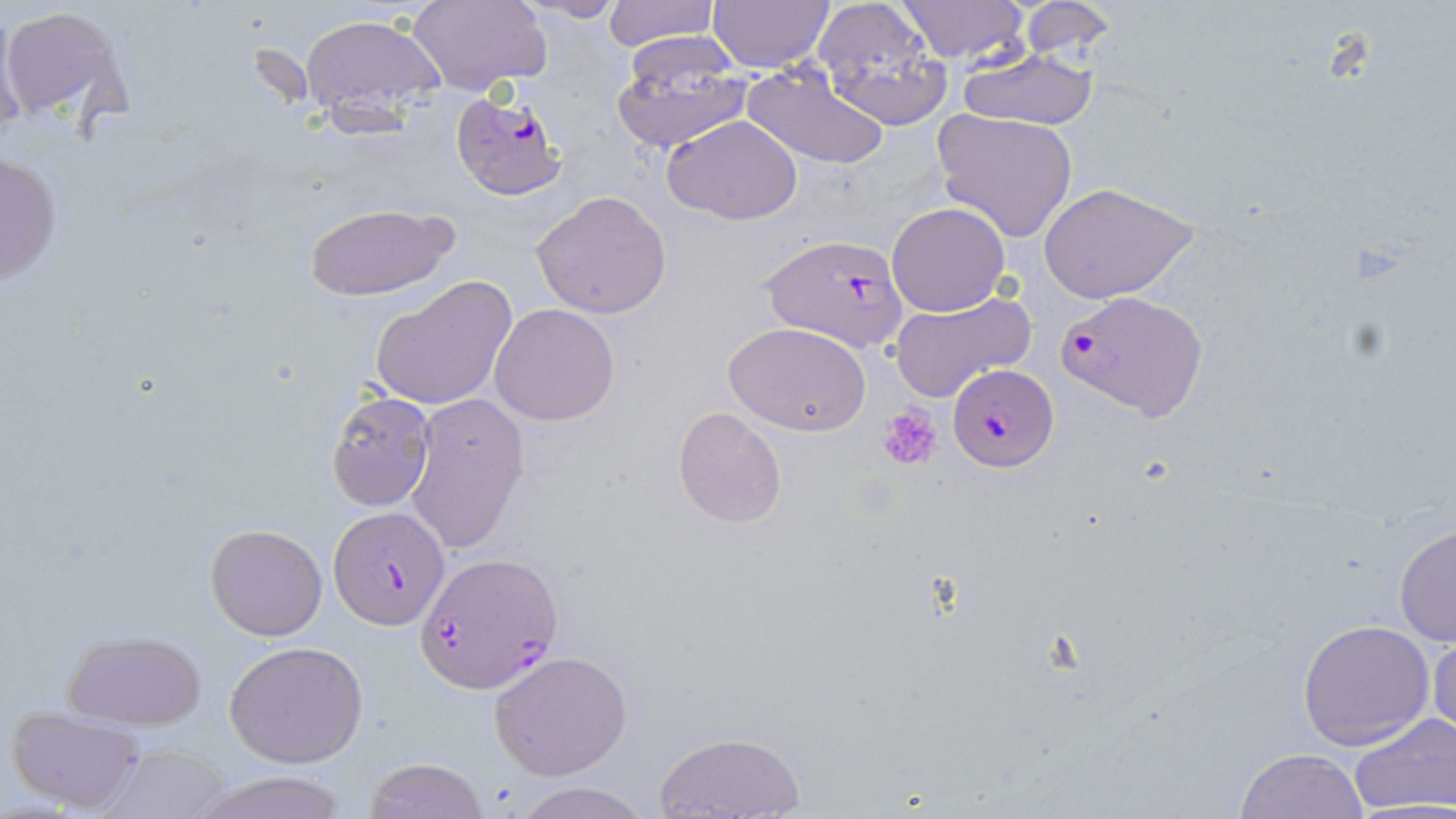
Summary:
  - Coordinate format: approximate bounding boxes as (x1, y1, x2, y2) in pixels
  - Platelet locations: (881, 405, 941, 471)
  - Uninfected red blood cell locations: (407, 0, 550, 94), (521, 0, 630, 23), (602, 0, 718, 51), (706, 0, 836, 72), (1019, 0, 1118, 62), (813, 1, 951, 130), (895, 1, 1032, 65), (1, 4, 134, 130), (301, 15, 443, 122), (610, 40, 749, 153), (956, 47, 1100, 130), (742, 62, 891, 168), (933, 110, 1077, 242), (664, 114, 802, 226), (1, 149, 64, 289), (1037, 182, 1197, 304), (532, 190, 673, 318), (886, 202, 1010, 317), (306, 203, 460, 303), (371, 273, 520, 411), (890, 290, 1035, 405), (490, 304, 619, 425), (724, 320, 873, 436), (323, 389, 437, 512), (405, 391, 530, 558), (672, 406, 787, 528), (1394, 519, 1456, 651), (204, 524, 327, 641), (1297, 619, 1436, 750), (1427, 622, 1456, 750), (61, 628, 206, 731), (225, 640, 369, 769), (488, 649, 632, 779), (7, 705, 147, 813), (1349, 711, 1454, 815), (655, 729, 805, 817), (96, 743, 235, 818), (1235, 746, 1369, 818), (362, 757, 491, 818), (187, 770, 355, 819), (509, 781, 655, 819)
  - Plasmodium falciparum-infected red blood cell locations: (451, 92, 566, 203), (759, 233, 910, 352), (1056, 288, 1211, 422), (948, 364, 1059, 472), (328, 506, 447, 629), (417, 551, 563, 691)
  - Slide-level diagnosis: Plasmodium falciparum
  - Modality: optical microscopy
  - Image size: 1456×819 pixels
  - Preparation: thin blood smear
  - Field of view: one of a larger specimen
  - Magnification: 1000x
  - Stain: May-Grünwald-Giemsa